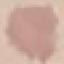
malaria_status: uninfected
stain: Giemsa
capture: smartphone through the microscope eyepiece
preparation: thin blood film
image_type: cell patch, automatically extracted from a larger field of view and resized to 64 × 64 pixels